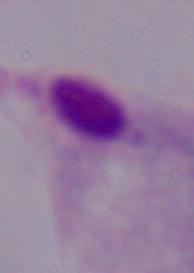

Captured at 1000x magnification. A trichomonad is shown. Micrograph.